Locate and identify every blood parasite.
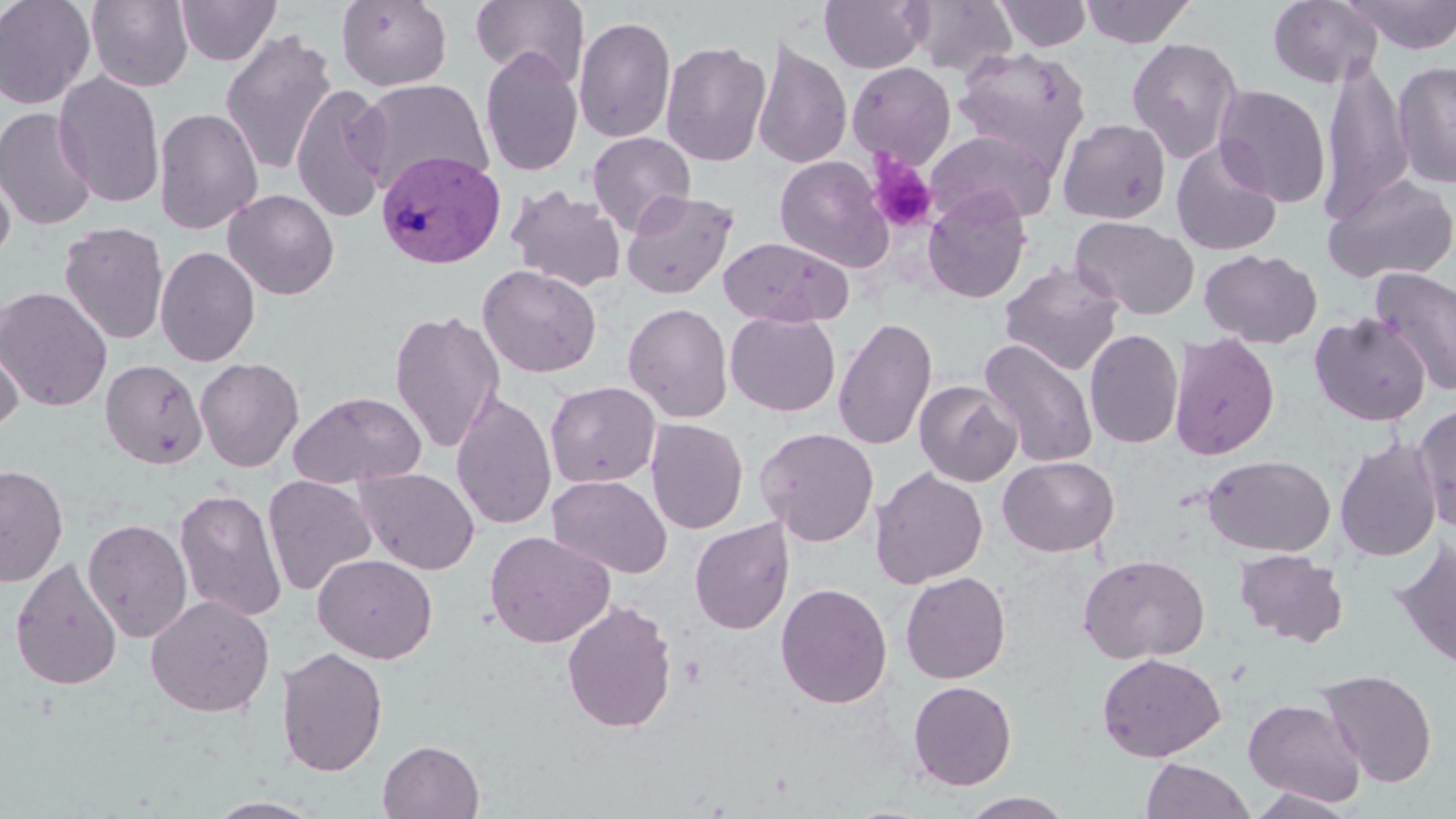
Approximate bounding boxes as [x1, y1, x2, y2] in pixels.
Plasmodium vivax-infected red blood cells: [376, 149, 507, 269].
No Plasmodium falciparum, Plasmodium ovale, Plasmodium malariae, Babesia divergens, or Trypanosoma brucei observed.

{
  "slide_level_diagnosis": "Plasmodium vivax",
  "field_of_view": "one of a larger specimen",
  "uninfected_red_blood_cell_locations": "approximate bounding boxes as [x1, y1, x2, y2] in pixels: [0, 0, 97, 110], [86, 0, 194, 91], [175, 0, 281, 66], [470, 0, 589, 85], [819, 0, 932, 73], [908, 0, 1019, 78], [993, 0, 1093, 51], [1080, 0, 1196, 48], [1268, 0, 1383, 88], [1344, 0, 1456, 54], [337, 1, 452, 91], [573, 14, 676, 144], [220, 28, 338, 177], [1126, 37, 1244, 163], [753, 39, 852, 170], [660, 40, 771, 167], [951, 46, 1092, 170], [479, 47, 584, 178], [1393, 59, 1456, 190], [1318, 60, 1414, 224], [847, 61, 956, 169], [53, 70, 165, 209], [355, 78, 493, 195], [291, 83, 392, 222], [1213, 84, 1332, 207], [0, 106, 98, 231], [153, 106, 264, 235], [1057, 117, 1171, 224], [926, 129, 1056, 227], [586, 131, 696, 235], [1169, 140, 1283, 255], [774, 154, 895, 272], [0, 162, 16, 268], [1323, 174, 1456, 285], [507, 185, 627, 293], [224, 189, 339, 300], [621, 189, 739, 299], [922, 189, 1032, 303], [1070, 215, 1200, 321], [59, 222, 169, 345], [719, 236, 853, 328], [155, 245, 259, 367], [1199, 248, 1322, 349], [999, 260, 1124, 375], [477, 264, 602, 378], [1370, 267, 1456, 397], [0, 286, 113, 412], [623, 302, 733, 422], [389, 308, 506, 453], [725, 311, 841, 417], [1309, 311, 1431, 426], [832, 317, 938, 451], [1083, 328, 1184, 449], [1169, 331, 1280, 460], [0, 333, 23, 435], [978, 338, 1099, 469], [195, 357, 304, 472], [100, 358, 208, 469], [914, 380, 1021, 487], [545, 381, 661, 488], [289, 390, 426, 488], [451, 390, 558, 532], [1412, 402, 1456, 532], [646, 418, 748, 534], [755, 426, 879, 546], [1335, 437, 1442, 560], [1202, 454, 1336, 557], [997, 455, 1120, 557], [0, 464, 68, 587], [870, 466, 989, 588], [354, 467, 481, 575], [547, 474, 672, 578], [262, 475, 377, 597], [174, 488, 287, 622], [82, 517, 193, 642], [689, 518, 794, 635], [484, 530, 615, 648], [1390, 538, 1456, 670], [1234, 549, 1348, 647], [313, 553, 437, 664], [1078, 554, 1210, 664], [9, 556, 124, 690], [900, 571, 1011, 684], [775, 582, 893, 709], [145, 594, 275, 717], [561, 598, 677, 734], [275, 646, 388, 776], [1096, 652, 1227, 762], [1317, 667, 1438, 788], [908, 680, 1017, 790], [1243, 698, 1366, 806], [378, 739, 484, 819], [1140, 758, 1255, 819], [1247, 789, 1362, 818], [958, 791, 1075, 819], [205, 797, 325, 818]",
  "modality": "light microscopy",
  "image_size": "1456×819 pixels",
  "magnification": "1000x",
  "stain": "May-Grünwald-Giemsa",
  "platelet_locations": "approximate bounding boxes as [x1, y1, x2, y2] in pixels: [866, 153, 938, 234]",
  "preparation": "thin blood smear"
}